Point out each Plasmodium parasite.
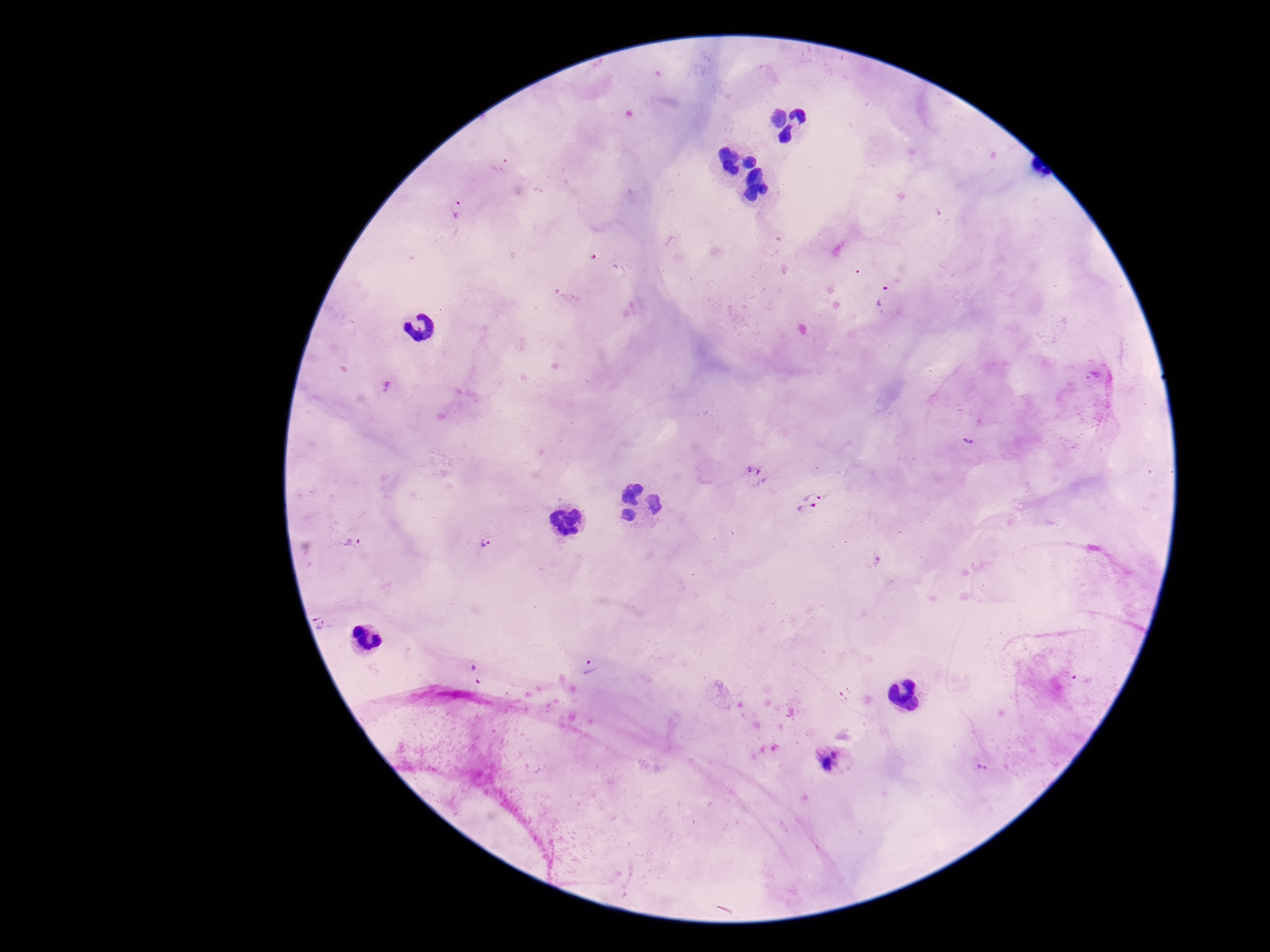

Approximate object centers, in pixels from the top-left corner.
Plasmodium parasites: (x=1091, y=376), (x=755, y=474), (x=812, y=489), (x=808, y=511), (x=352, y=541), (x=486, y=541), (x=835, y=758), (x=983, y=767).

Summary:
  - Image size: 1270×952 pixels
  - Field of view: one from this slide
  - Capture: smartphone camera through the microscope eyepiece
  - Preparation: thick blood film
  - Magnification: 100x
  - Stain: Giemsa
  - Patient malaria status: positive